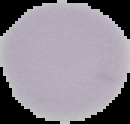

Image is 130×124 pixels. The area outside the segmented cell region is set to black. From a thin blood smear. Malaria status: uninfected.